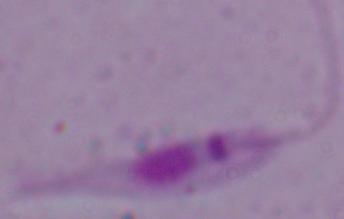

Summary:
  - Magnification: 1000x
  - Identification: Leishmania
  - Modality: photomicrograph